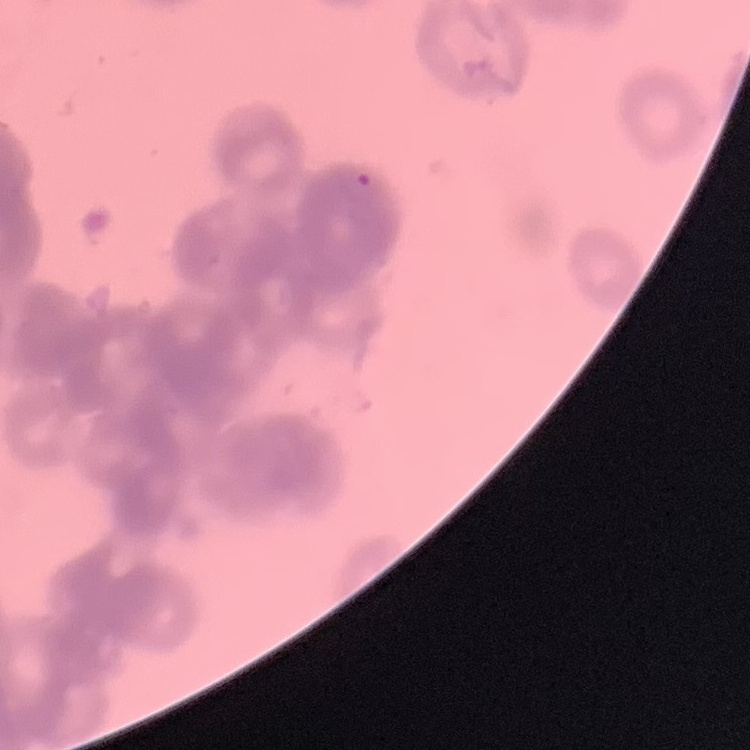

erythrocyte morphology = rouleaux formation
stain = Field's or Giemsa
preparation = thin blood film
image type = square crop of a larger photomicrograph